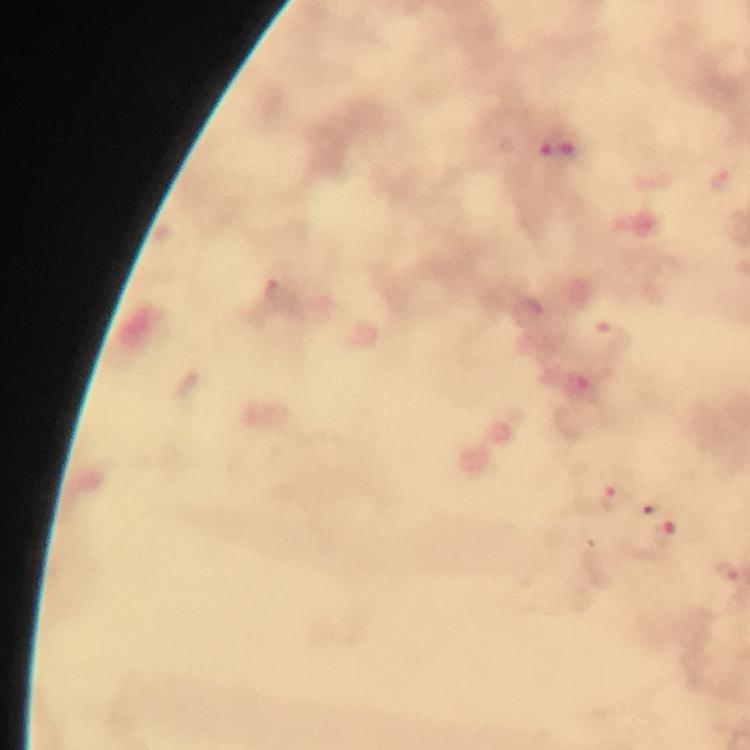
Approximate object centers, in pixels from the top-left corner. Malaria parasite locations: (x=541, y=150), (x=566, y=155), (x=278, y=294), (x=614, y=497), (x=659, y=505), (x=664, y=534), (x=725, y=572). 100x magnification. Thick blood smear. Smartphone photograph taken through a microscope. Image is 750×750 pixels. Immersion oil was used. Giemsa stain. Cropped region of a single field of view. From a malaria diagnostic workup.